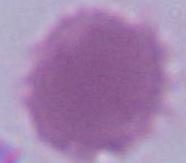
Summary:
  - Identification: erythrocyte
  - Modality: micrograph
  - Magnification: 1000x